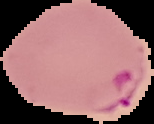
Summary:
  - Preparation: thin blood smear
  - Image size: 154×124 pixels
  - Result: malaria parasites identified
  - Image type: cell region segmented out of the field of view; surrounding area masked to black